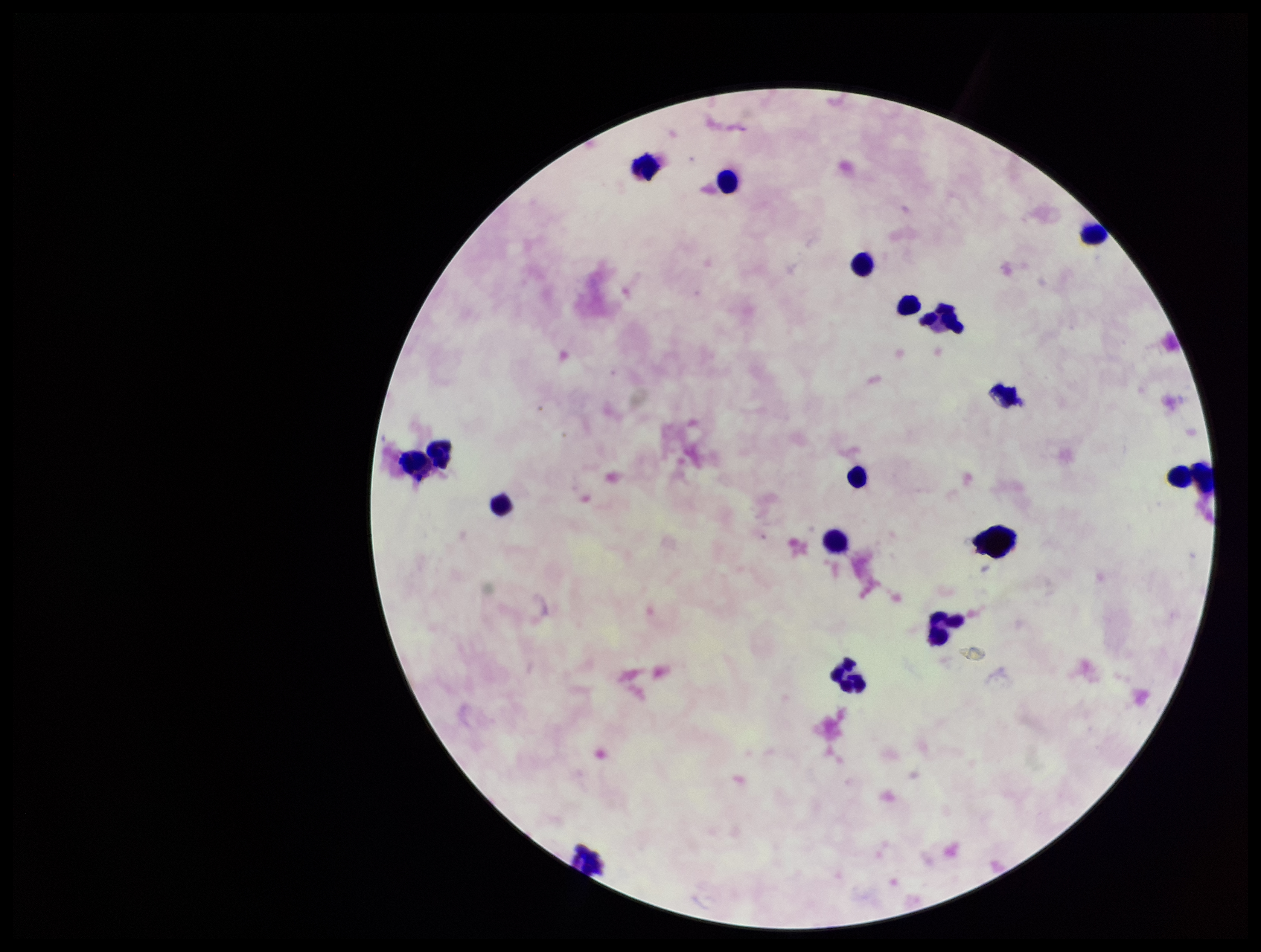

Summary:
  - Field of view: single
  - Stain: Giemsa
  - Preparation: thick
  - Patient malaria status: negative
  - Capture: smartphone photograph through the microscope eyepiece
  - Image size: 1261×952 pixels
  - Parasite count: 0
  - Leukocyte count: 16
  - Plasmodium parasites: none identified